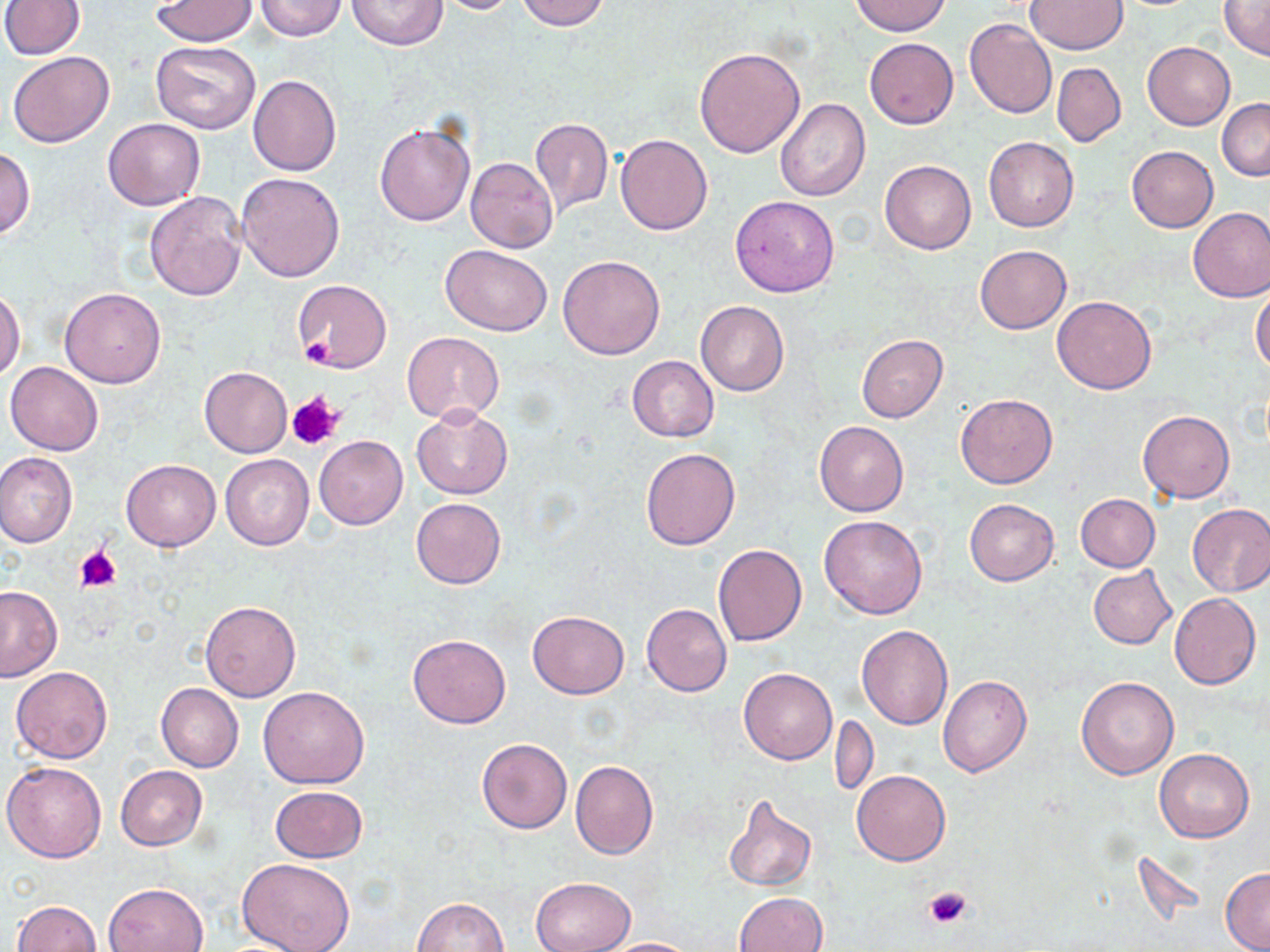 Approximate bounding boxes as (x1, y1, x2, y2) in pixels. Uninfected red blood cell locations: (253, 0, 348, 40), (345, 0, 449, 50), (433, 0, 524, 15), (513, 0, 610, 31), (0, 1, 84, 58), (153, 1, 257, 46), (850, 1, 950, 36), (1024, 1, 1127, 54), (1219, 1, 1270, 59), (964, 18, 1057, 118), (864, 38, 959, 129), (1143, 41, 1235, 130), (152, 42, 260, 135), (694, 47, 806, 158), (7, 50, 115, 148), (1052, 62, 1125, 146), (247, 74, 341, 176), (1218, 98, 1270, 180), (774, 99, 869, 201), (103, 117, 205, 210), (529, 117, 614, 219), (373, 119, 475, 226), (528, 126, 709, 224), (615, 135, 713, 236), (984, 136, 1078, 231), (1127, 145, 1218, 232), (0, 148, 34, 238), (465, 157, 558, 253), (880, 159, 976, 254), (237, 172, 346, 282), (144, 191, 247, 300), (730, 195, 839, 297), (1188, 207, 1270, 302), (440, 244, 551, 335), (974, 244, 1072, 335), (557, 255, 665, 360), (292, 278, 391, 373), (1251, 286, 1270, 374), (59, 287, 167, 388), (1, 288, 24, 381), (1052, 295, 1156, 394), (695, 301, 789, 395), (402, 332, 505, 423), (857, 335, 948, 422), (626, 356, 718, 442), (5, 362, 104, 456), (198, 366, 291, 458), (955, 393, 1057, 488), (412, 406, 512, 498), (1137, 410, 1235, 502), (814, 421, 909, 516), (314, 436, 408, 529), (641, 447, 740, 550), (0, 452, 77, 548), (220, 454, 314, 549), (120, 459, 220, 551), (1074, 494, 1161, 572), (411, 497, 506, 589), (964, 499, 1059, 585), (1187, 503, 1270, 597), (819, 515, 929, 619), (712, 544, 806, 647), (1088, 566, 1177, 648), (0, 585, 63, 681), (1169, 592, 1261, 689), (199, 600, 300, 702), (641, 603, 732, 697), (527, 610, 629, 699), (856, 625, 953, 730), (408, 634, 511, 728), (11, 667, 112, 764), (739, 668, 837, 765), (937, 675, 1032, 777), (1076, 677, 1179, 780), (156, 683, 244, 772), (257, 686, 369, 789), (830, 713, 878, 799), (476, 738, 573, 834), (1154, 748, 1255, 843), (570, 760, 659, 859), (3, 761, 107, 863), (115, 765, 207, 850), (852, 770, 950, 865), (271, 787, 367, 862), (722, 793, 818, 891), (236, 858, 356, 952), (1221, 867, 1270, 951), (530, 877, 634, 952), (102, 883, 209, 952), (735, 892, 828, 952), (411, 898, 510, 952), (12, 899, 103, 951), (600, 937, 698, 952). Platelet locations: (303, 339, 335, 366), (286, 391, 344, 451), (76, 547, 121, 592), (923, 886, 973, 930). Slide-level diagnosis: negative for blood parasites. Thin blood film. Single field of view. 1000x magnification. Image is 1270×952 pixels. Optical microscopy. May-Grünwald-Giemsa stain.